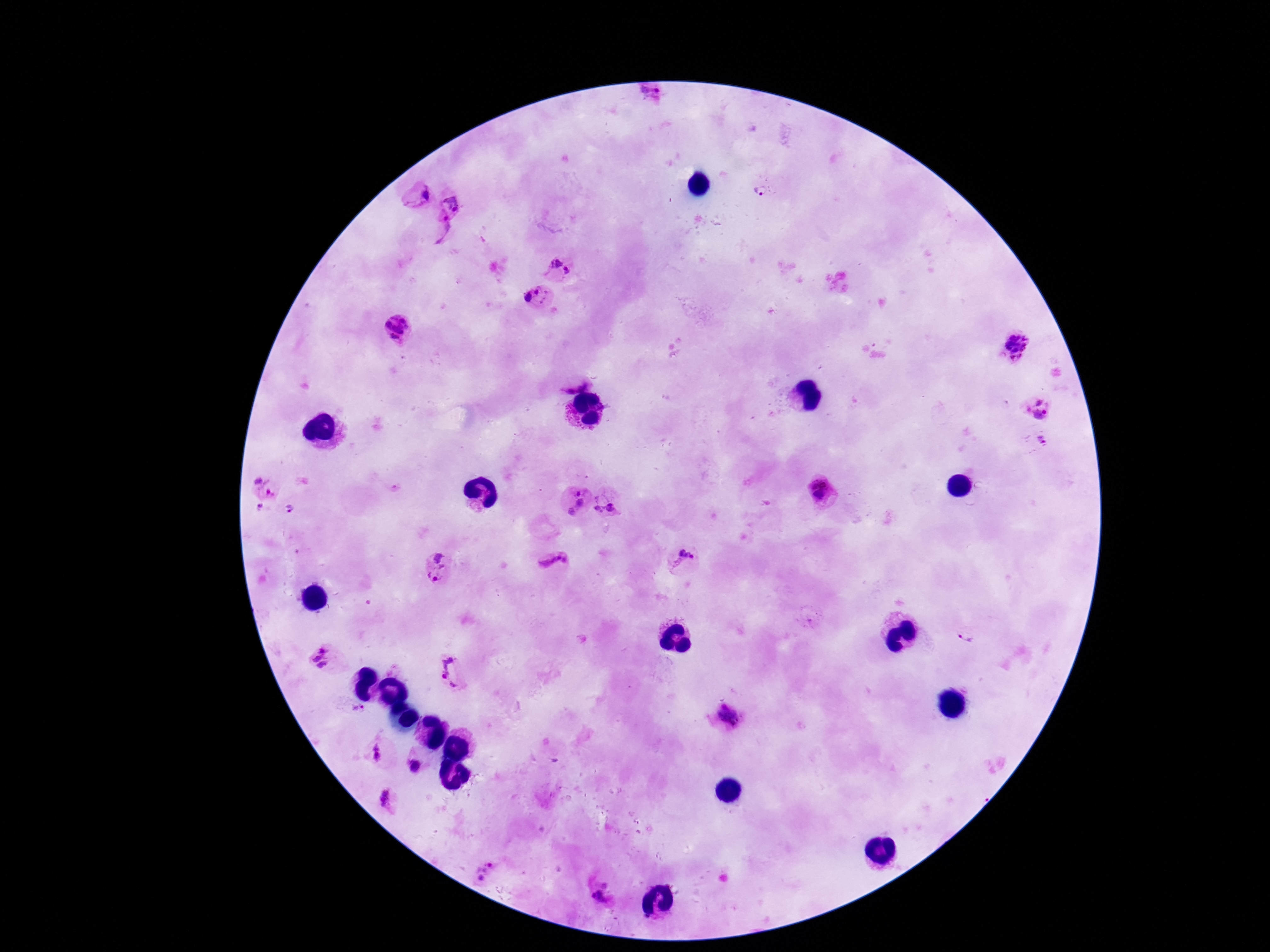
{
  "image_size": "1270×952 pixels",
  "preparation": "thick blood smear",
  "field_of_view": "single",
  "magnification": "100x",
  "capture": "smartphone camera through the microscope eyepiece",
  "plasmodium_parasite_locations": "approximate centers as [x, y] in pixels: [651, 94], [761, 190], [425, 195], [454, 202], [440, 227], [556, 261], [567, 271], [539, 290], [527, 297], [400, 328], [1015, 344], [575, 377], [1038, 400], [1041, 416], [1041, 440], [265, 486], [820, 490], [578, 492], [580, 504], [611, 505], [259, 509], [598, 509], [290, 510], [569, 513], [686, 551], [554, 564], [434, 565], [966, 638], [319, 659], [456, 669], [358, 710], [729, 717], [378, 753], [415, 766], [386, 799], [486, 872], [600, 897]",
  "patient_malaria_status": "positive",
  "stain": "Giemsa"
}